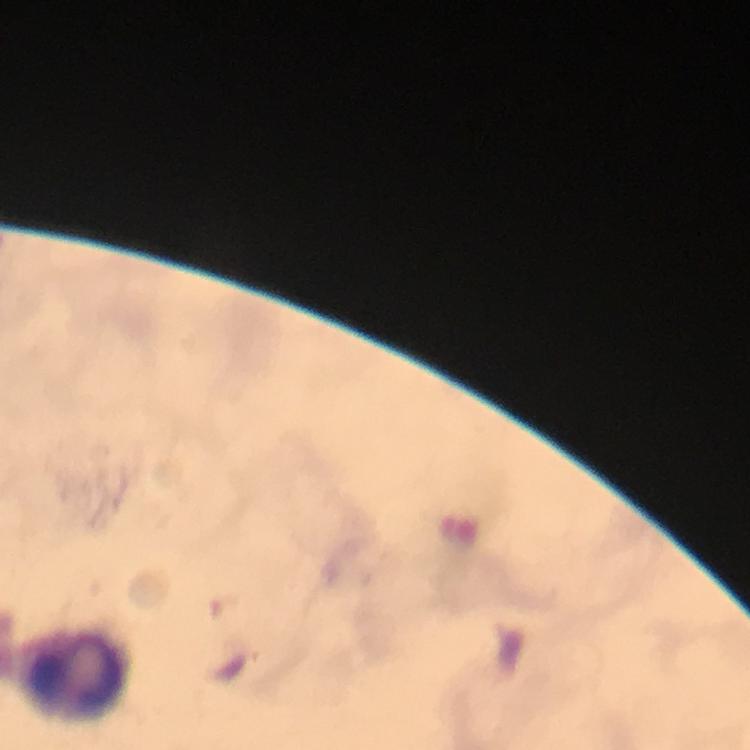
Approximate centers as (x, y) in pixels.
Summary:
  - Leukocyte locations: (72, 674)
  - Context: from a diagnostic examination for malaria
  - Immersion oil: applied
  - Magnification: 100x
  - Stain: Giemsa
  - Capture: smartphone camera through the microscope
  - Preparation: thick smear
  - Plasmodium parasites: none detected
  - Cropped from: a single field of view
  - Image size: 750×750 pixels